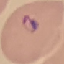
result = malaria parasites detected
preparation = thin blood film
image type = cell patch, automatically extracted from a larger field of view and resized to 64 × 64 pixels
capture = smartphone through the microscope eyepiece
stain = Giemsa